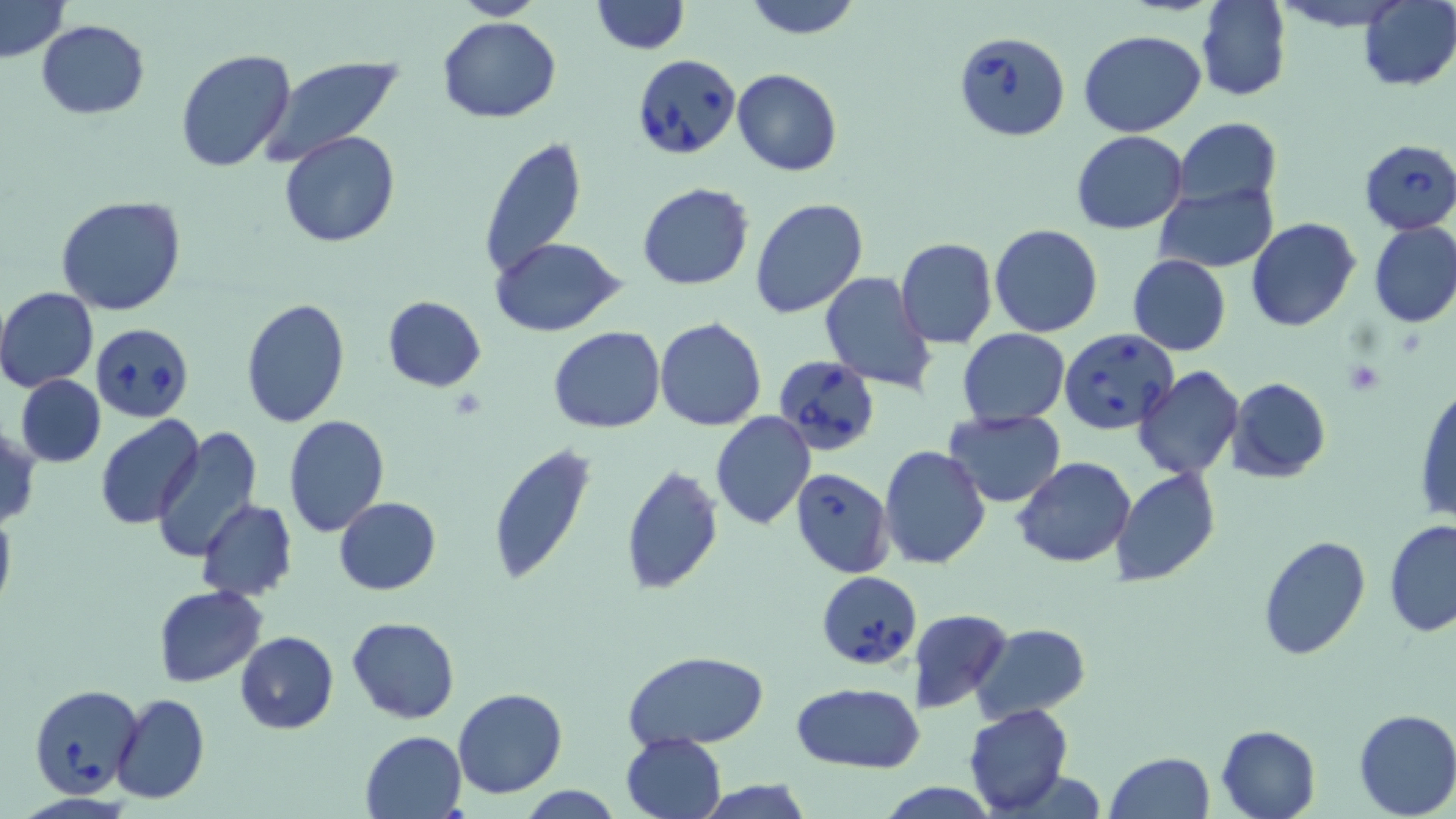

slide_level_diagnosis: Babesia divergens
image_size: 1456×819 pixels
preparation: thin blood film
magnification: 1000x
modality: optical microscopy
babesia_divergens_infected_red_blood_cell_locations: 'approximate bounding boxes as (x1,y1)-(x2,y2) corner pairs in pixels: (954,31)-(1072,141), (630,52)-(740,160), (1357,138)-(1456,234), (91,324)-(194,420), (1060,328)-(1177,435), (774,357)-(879,457), (791,467)-(894,578), (816,570)-(921,669), (28,683)-(144,797)'
platelet_locations: 'approximate bounding boxes as (x1,y1)-(x2,y2) corner pairs in pixels: (1346,360)-(1385,394)'
stain: May-Grünwald-Giemsa
uninfected_red_blood_cell_locations: 'approximate bounding boxes as (x1,y1)-(x2,y2) corner pairs in pixels: (449,0)-(549,20), (590,0)-(689,54), (740,0)-(865,39), (1197,0)-(1291,101), (1271,0)-(1412,30), (1,1)-(71,61), (1357,1)-(1456,90), (439,17)-(561,122), (35,18)-(150,119), (1079,30)-(1207,138), (175,48)-(297,174), (255,54)-(405,167), (732,69)-(842,178), (1174,118)-(1282,208), (1071,130)-(1188,235), (278,131)-(402,248), (479,135)-(586,283), (1155,182)-(1278,273), (637,183)-(754,291), (56,195)-(188,315), (749,198)-(868,318), (1246,217)-(1361,332), (1367,220)-(1456,329), (990,223)-(1103,337), (894,237)-(998,348), (490,238)-(625,337), (1127,254)-(1231,356), (821,270)-(938,395), (0,287)-(98,392), (381,295)-(487,392), (241,298)-(350,428), (654,316)-(767,430), (550,326)-(665,434), (957,329)-(1071,426), (1132,366)-(1245,479), (15,375)-(106,469), (1228,377)-(1330,481), (1413,383)-(1456,526), (944,409)-(1067,507), (711,411)-(816,530), (284,415)-(389,537), (96,416)-(204,530), (0,423)-(40,530), (149,428)-(263,560), (486,442)-(595,585), (878,445)-(992,571), (1013,456)-(1137,569), (620,464)-(725,595), (1112,467)-(1219,588), (333,496)-(441,596), (195,500)-(298,603), (0,509)-(15,616), (1384,517)-(1456,636), (1257,535)-(1370,660), (154,585)-(266,686), (906,609)-(1013,713), (347,615)-(459,723), (972,623)-(1091,722), (236,631)-(338,733), (623,650)-(770,751), (793,683)-(924,772), (452,687)-(567,799), (111,692)-(209,804), (963,705)-(1073,815), (1353,708)-(1456,818), (1217,724)-(1321,819), (359,730)-(467,818), (621,731)-(726,818), (1105,751)-(1215,819), (693,779)-(816,819), (875,781)-(1000,817), (514,786)-(628,819)'
field_of_view: single